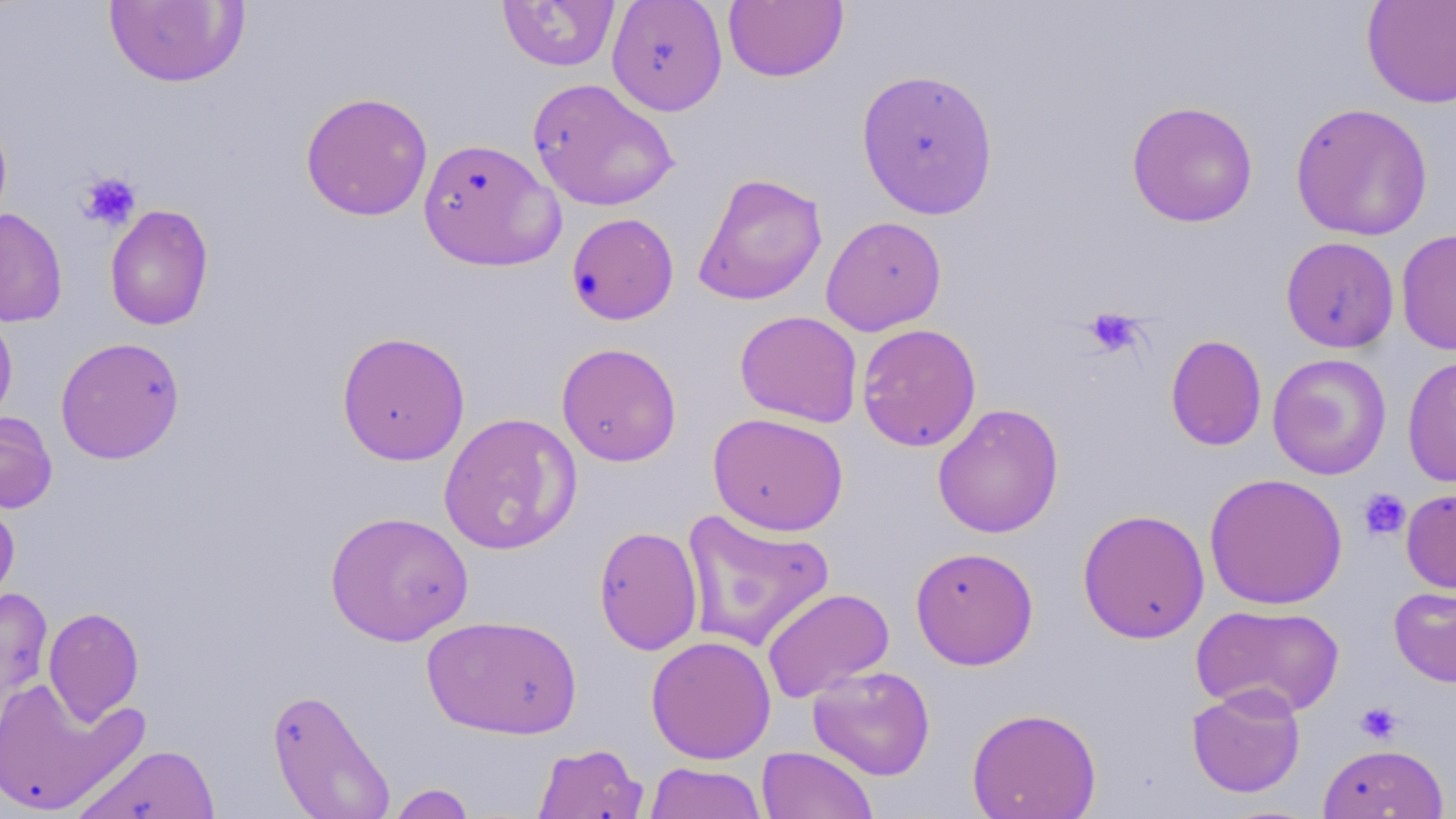

slide_level_diagnosis: negative for blood parasites
modality: optical microscopy
platelet_locations: 'approximate bounding boxes as named x1/y1/x2/y2 corners in pixels: (x1=77, y1=172, x2=141, y2=231), (x1=1083, y1=308, x2=1143, y2=358), (x1=1358, y1=488, x2=1411, y2=541), (x1=1355, y1=701, x2=1403, y2=743)'
stain: May-Grünwald-Giemsa
uninfected_red_blood_cell_locations: 'approximate bounding boxes as named x1/y1/x2/y2 corners in pixels: (x1=104, y1=0, x2=248, y2=87), (x1=607, y1=0, x2=728, y2=115), (x1=1361, y1=0, x2=1456, y2=109), (x1=497, y1=1, x2=620, y2=72), (x1=723, y1=1, x2=848, y2=82), (x1=856, y1=67, x2=999, y2=220), (x1=527, y1=77, x2=679, y2=211), (x1=300, y1=91, x2=433, y2=221), (x1=1126, y1=100, x2=1259, y2=227), (x1=1290, y1=102, x2=1433, y2=241), (x1=0, y1=111, x2=13, y2=232), (x1=418, y1=138, x2=565, y2=272), (x1=692, y1=172, x2=828, y2=306), (x1=104, y1=204, x2=214, y2=331), (x1=0, y1=207, x2=68, y2=327), (x1=566, y1=212, x2=679, y2=326), (x1=820, y1=215, x2=947, y2=336), (x1=1395, y1=228, x2=1456, y2=356), (x1=1281, y1=236, x2=1399, y2=353), (x1=0, y1=307, x2=18, y2=429), (x1=734, y1=310, x2=863, y2=427), (x1=856, y1=323, x2=982, y2=451), (x1=336, y1=331, x2=471, y2=465), (x1=1165, y1=334, x2=1267, y2=452), (x1=55, y1=336, x2=185, y2=464), (x1=556, y1=342, x2=682, y2=467), (x1=1267, y1=353, x2=1392, y2=480), (x1=1402, y1=355, x2=1456, y2=488), (x1=932, y1=403, x2=1064, y2=538), (x1=0, y1=410, x2=58, y2=514), (x1=438, y1=412, x2=582, y2=555), (x1=707, y1=412, x2=849, y2=536), (x1=1204, y1=472, x2=1348, y2=610), (x1=1401, y1=487, x2=1456, y2=594), (x1=0, y1=496, x2=20, y2=613), (x1=1077, y1=508, x2=1210, y2=644), (x1=680, y1=509, x2=835, y2=652), (x1=325, y1=510, x2=473, y2=646), (x1=593, y1=525, x2=704, y2=656), (x1=910, y1=546, x2=1039, y2=670), (x1=1388, y1=584, x2=1456, y2=687), (x1=0, y1=586, x2=53, y2=746), (x1=761, y1=587, x2=895, y2=703), (x1=1191, y1=603, x2=1345, y2=718), (x1=43, y1=606, x2=144, y2=724), (x1=422, y1=614, x2=583, y2=739), (x1=646, y1=635, x2=777, y2=764), (x1=807, y1=665, x2=936, y2=780), (x1=0, y1=677, x2=147, y2=815), (x1=1187, y1=684, x2=1306, y2=798), (x1=267, y1=687, x2=396, y2=818), (x1=966, y1=707, x2=1102, y2=819), (x1=532, y1=742, x2=648, y2=819), (x1=72, y1=743, x2=222, y2=819), (x1=1317, y1=743, x2=1449, y2=818), (x1=756, y1=745, x2=878, y2=819), (x1=644, y1=762, x2=767, y2=819), (x1=385, y1=783, x2=476, y2=819)'
field_of_view: single
magnification: 1000x
preparation: thin blood film
image_size: 1456×819 pixels